Name the parasite shown.
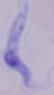

A trypanosome.

1000x magnification. Micrograph.